State which parasite is depicted.
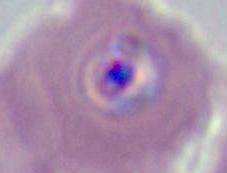

Plasmodium.

Summary:
  - Magnification: 400x or 1000x
  - Modality: micrograph